Comment on the morphology of the erythrocytes.
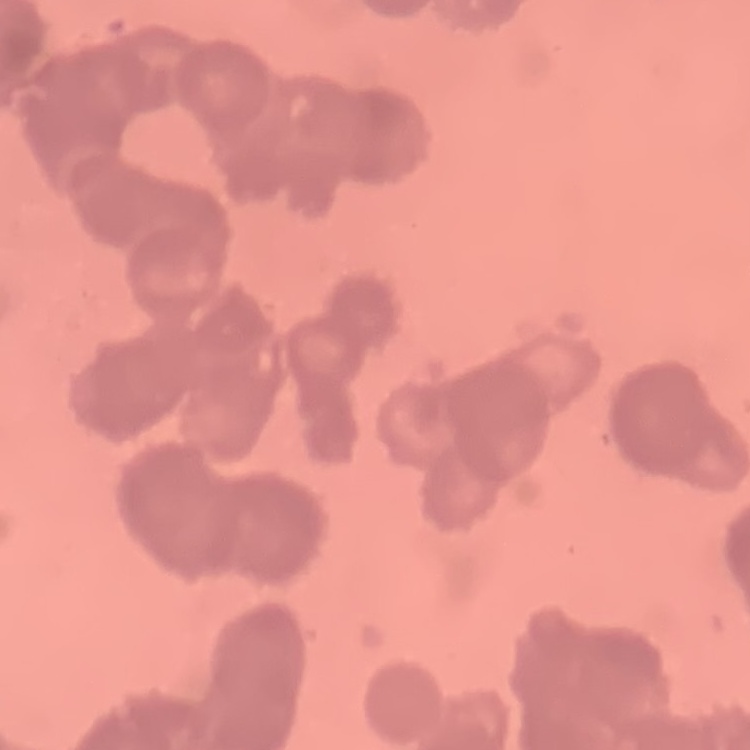
Rouleaux formation.

One tile cut from a larger photomicrograph. Field's or Giemsa stain. Thin blood film.